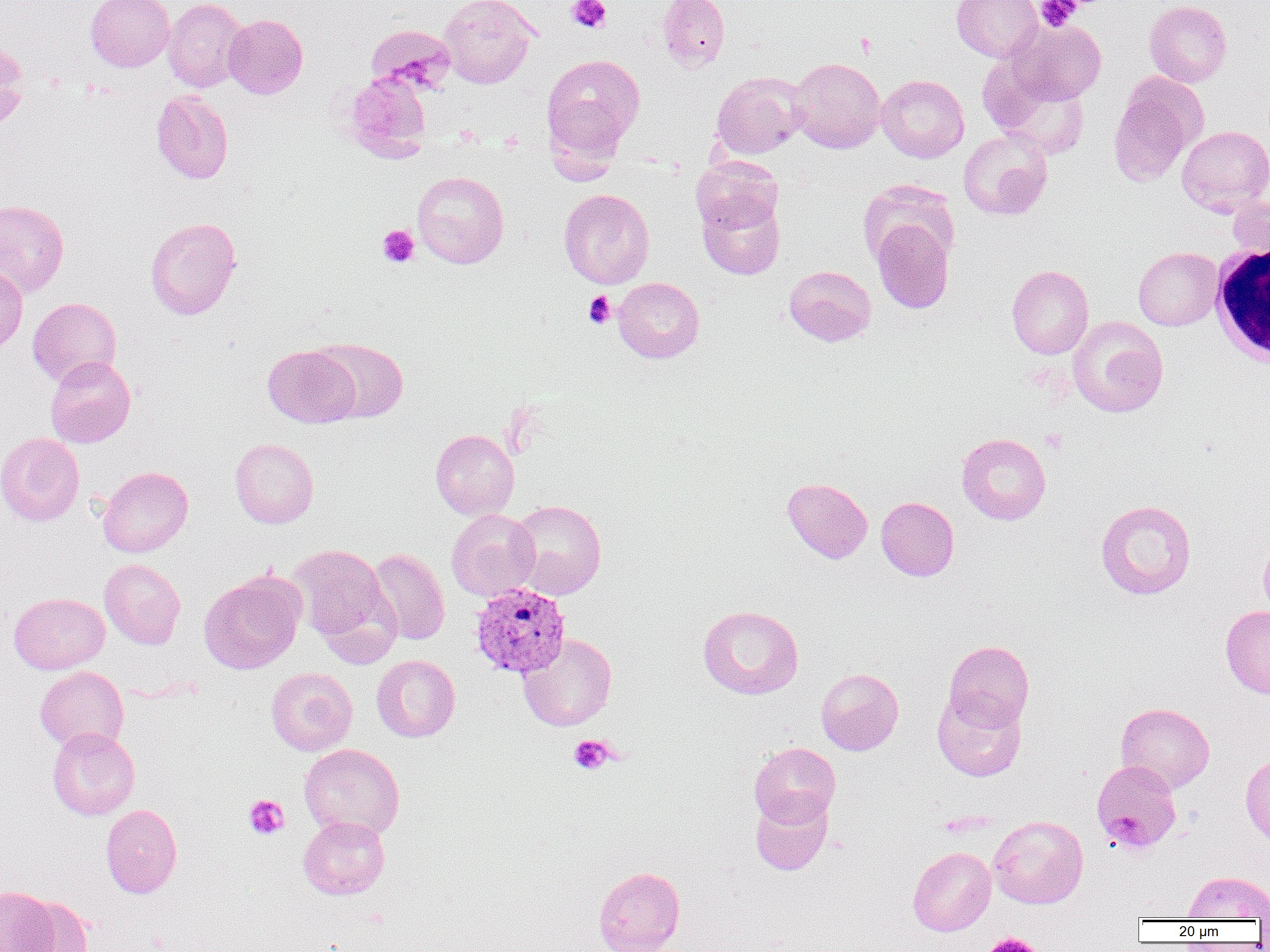

slide-level diagnosis = Plasmodium vivax
uninfected red blood cell locations = approximate bounding boxes as named x1/y1/x2/y2 corners in pixels: (x1=85, y1=0, x2=174, y2=71), (x1=163, y1=0, x2=248, y2=92), (x1=438, y1=0, x2=538, y2=89), (x1=657, y1=0, x2=730, y2=71), (x1=952, y1=0, x2=1042, y2=62), (x1=1145, y1=1, x2=1232, y2=87), (x1=224, y1=14, x2=308, y2=99), (x1=1006, y1=19, x2=1106, y2=106), (x1=365, y1=25, x2=456, y2=95), (x1=0, y1=41, x2=29, y2=131), (x1=542, y1=54, x2=645, y2=158), (x1=788, y1=57, x2=886, y2=153), (x1=984, y1=65, x2=1090, y2=158), (x1=711, y1=71, x2=808, y2=159), (x1=341, y1=72, x2=432, y2=163), (x1=876, y1=74, x2=969, y2=162), (x1=1108, y1=77, x2=1203, y2=188), (x1=151, y1=90, x2=234, y2=184), (x1=1177, y1=125, x2=1270, y2=214), (x1=958, y1=129, x2=1053, y2=220), (x1=693, y1=159, x2=783, y2=234), (x1=412, y1=171, x2=509, y2=268), (x1=859, y1=179, x2=959, y2=270), (x1=558, y1=188, x2=654, y2=289), (x1=697, y1=190, x2=786, y2=280), (x1=1226, y1=193, x2=1270, y2=260), (x1=0, y1=199, x2=69, y2=297), (x1=145, y1=217, x2=241, y2=320), (x1=872, y1=220, x2=954, y2=313), (x1=1133, y1=247, x2=1222, y2=330), (x1=0, y1=264, x2=28, y2=355), (x1=784, y1=265, x2=876, y2=346), (x1=1007, y1=265, x2=1093, y2=359), (x1=613, y1=277, x2=704, y2=363), (x1=27, y1=297, x2=122, y2=387), (x1=1068, y1=316, x2=1168, y2=417), (x1=309, y1=337, x2=409, y2=423), (x1=263, y1=345, x2=360, y2=428), (x1=44, y1=356, x2=136, y2=448), (x1=430, y1=429, x2=519, y2=520), (x1=0, y1=432, x2=85, y2=526), (x1=957, y1=433, x2=1051, y2=525), (x1=230, y1=437, x2=319, y2=528), (x1=98, y1=466, x2=193, y2=557), (x1=782, y1=477, x2=872, y2=563), (x1=876, y1=496, x2=959, y2=580), (x1=509, y1=499, x2=607, y2=600), (x1=1096, y1=500, x2=1196, y2=599), (x1=446, y1=509, x2=539, y2=601), (x1=1259, y1=537, x2=1270, y2=623), (x1=288, y1=545, x2=392, y2=647), (x1=365, y1=549, x2=450, y2=645), (x1=99, y1=558, x2=186, y2=649), (x1=199, y1=569, x2=306, y2=674), (x1=8, y1=592, x2=110, y2=674), (x1=697, y1=605, x2=804, y2=699), (x1=1221, y1=605, x2=1270, y2=698), (x1=518, y1=634, x2=617, y2=732), (x1=943, y1=640, x2=1034, y2=730), (x1=372, y1=655, x2=460, y2=742), (x1=35, y1=666, x2=129, y2=753), (x1=266, y1=667, x2=358, y2=755), (x1=816, y1=668, x2=903, y2=755), (x1=932, y1=688, x2=1027, y2=782), (x1=1116, y1=703, x2=1215, y2=793), (x1=47, y1=727, x2=140, y2=820), (x1=749, y1=742, x2=840, y2=827), (x1=299, y1=743, x2=405, y2=839), (x1=1240, y1=753, x2=1270, y2=847), (x1=750, y1=793, x2=833, y2=875), (x1=100, y1=804, x2=182, y2=898), (x1=988, y1=815, x2=1088, y2=908), (x1=298, y1=816, x2=390, y2=899), (x1=908, y1=847, x2=996, y2=936), (x1=593, y1=866, x2=685, y2=952), (x1=1183, y1=871, x2=1270, y2=920), (x1=0, y1=885, x2=59, y2=951), (x1=14, y1=896, x2=93, y2=952)
field of view = one of a larger specimen
preparation = thin blood film
modality = optical microscopy
platelet locations = approximate bounding boxes as named x1/y1/x2/y2 corners in pixels: (x1=567, y1=0, x2=611, y2=33), (x1=1035, y1=0, x2=1081, y2=31), (x1=854, y1=32, x2=877, y2=57), (x1=377, y1=225, x2=419, y2=268), (x1=583, y1=291, x2=616, y2=328), (x1=1040, y1=429, x2=1068, y2=453), (x1=568, y1=735, x2=616, y2=775), (x1=244, y1=795, x2=289, y2=839), (x1=983, y1=932, x2=1045, y2=952)
white blood cell locations = approximate bounding boxes as named x1/y1/x2/y2 corners in pixels: (x1=1209, y1=242, x2=1270, y2=368)
image size = 1270×952 pixels
Plasmodium vivax-infected red blood cell locations = approximate bounding boxes as named x1/y1/x2/y2 corners in pixels: (x1=469, y1=581, x2=570, y2=678), (x1=1092, y1=760, x2=1182, y2=854)
magnification = 1000x